Name the blood parasite species.
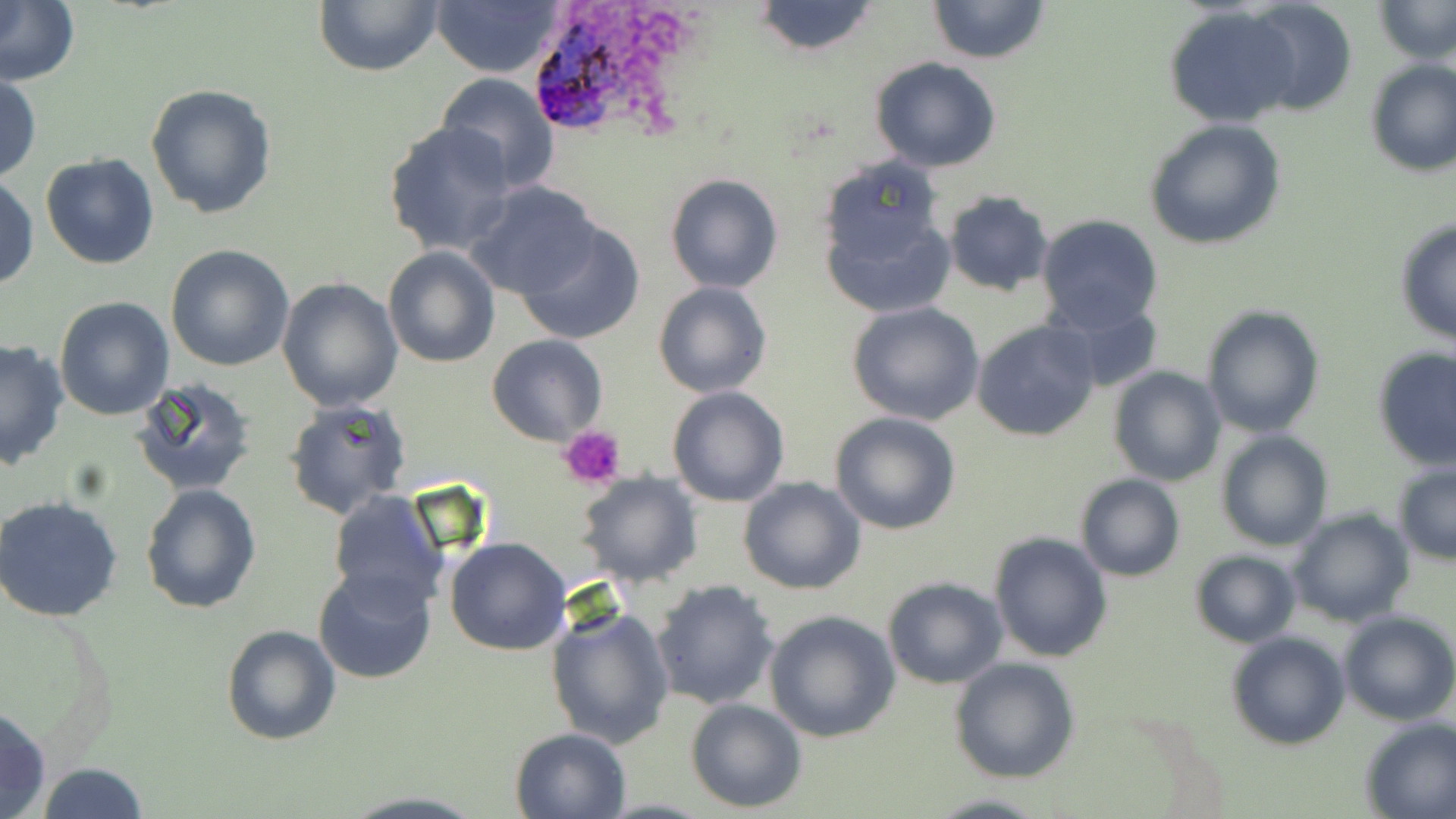

Plasmodium ovale.

Approximate bounding boxes as (x1, y1, x2, y2) in pixels. Platelet locations: (560, 423, 626, 490). Uninfected red blood cell locations: (0, 0, 80, 88), (750, 0, 883, 56), (926, 0, 1051, 65), (1376, 0, 1456, 65), (314, 1, 445, 77), (1242, 1, 1358, 116), (433, 2, 565, 77), (1162, 8, 1299, 127), (868, 56, 1001, 172), (1363, 58, 1456, 176), (434, 71, 559, 193), (0, 73, 41, 183), (145, 83, 276, 219), (1145, 119, 1288, 251), (382, 121, 517, 257), (41, 154, 161, 271), (664, 172, 783, 294), (1, 177, 38, 290), (819, 180, 955, 316), (464, 181, 604, 302), (944, 190, 1054, 296), (1036, 213, 1164, 335), (1394, 218, 1455, 345), (516, 220, 646, 344), (165, 243, 294, 372), (383, 246, 500, 367), (276, 276, 403, 410), (653, 281, 772, 397), (55, 298, 173, 421), (1053, 298, 1166, 395), (846, 302, 987, 427), (1201, 305, 1325, 437), (972, 317, 1103, 442), (486, 334, 608, 446), (0, 338, 70, 470), (1372, 345, 1456, 470), (1107, 366, 1227, 486), (131, 378, 257, 496), (667, 386, 790, 507), (284, 398, 411, 520), (830, 410, 962, 535), (1216, 429, 1331, 551), (1393, 465, 1456, 565), (577, 473, 702, 587), (1075, 473, 1185, 582), (738, 476, 866, 595), (140, 482, 263, 614), (326, 489, 449, 612), (0, 495, 125, 623), (1289, 509, 1414, 628), (989, 531, 1112, 663), (444, 536, 572, 656), (1189, 548, 1301, 648), (313, 567, 437, 683), (882, 576, 1009, 689), (651, 579, 781, 710), (911, 604, 1048, 750), (544, 606, 675, 750), (764, 609, 900, 743), (1338, 609, 1456, 726), (221, 625, 342, 746), (1227, 631, 1349, 750), (950, 657, 1080, 784), (686, 698, 808, 814), (0, 704, 50, 819), (1358, 717, 1456, 819), (509, 726, 630, 818), (35, 763, 149, 819), (926, 793, 1047, 819). Plasmodium ovale-infected red blood cell locations: (522, 9, 636, 133). Image is 1456×819 pixels. Light microscopy. Captured at 1000x magnification. One field of a larger specimen. Thin blood smear. May-Grünwald-Giemsa stain.